Give the position of every Plasmodium parasite visible.
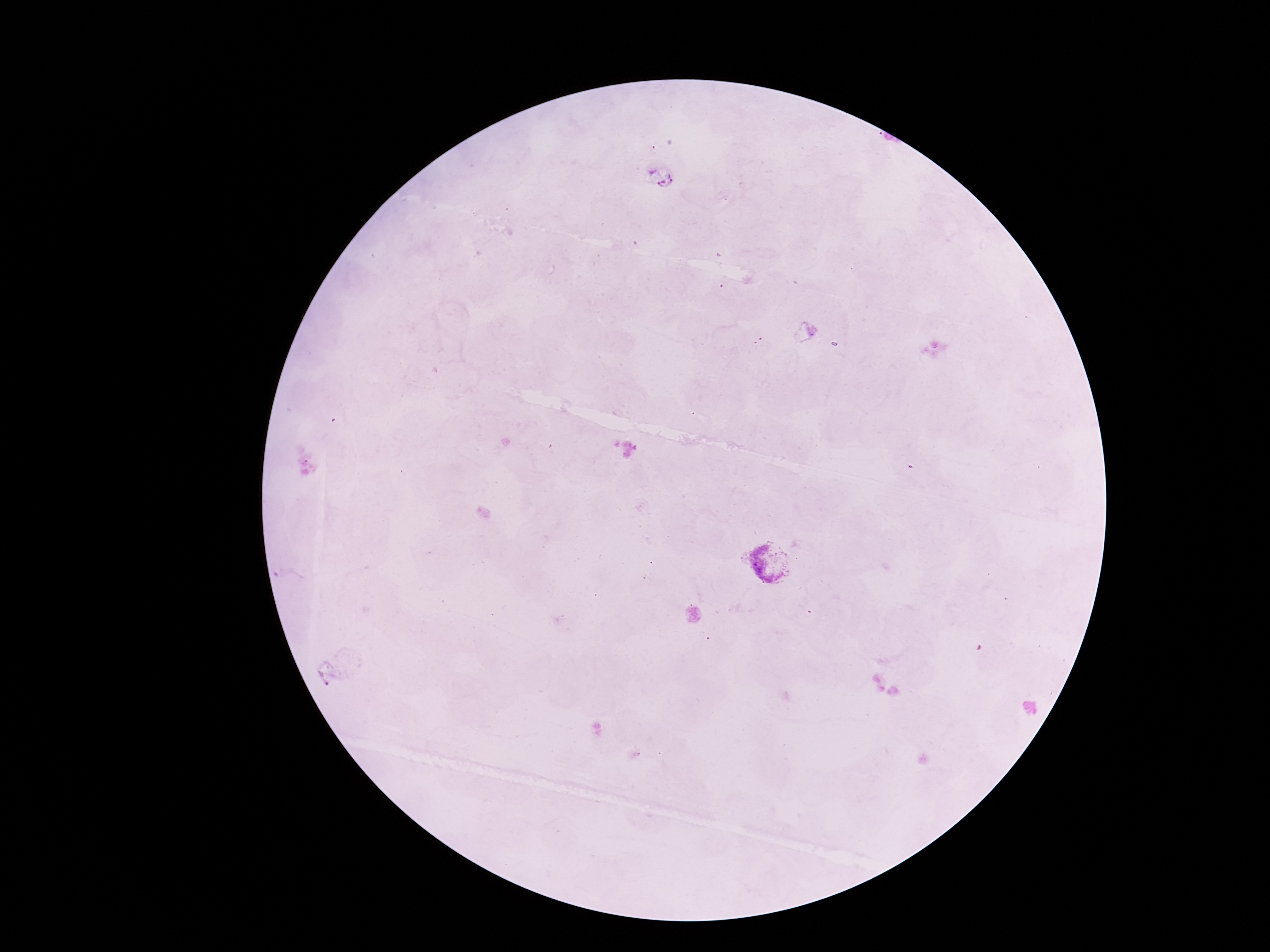
Approximate centers as {x, y} in pixels.
Plasmodium parasites: {662, 175}, {770, 561}.

Summary:
  - Capture: smartphone camera through the microscope eyepiece
  - Image size: 1270×952 pixels
  - Magnification: 100x
  - Preparation: thick blood smear
  - Stain: Giemsa
  - Field of view: one from this slide
  - Patient malaria status: positive